Classify this cell by malaria status.
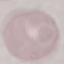

Uninfected.

Summary:
  - Image type: cell patch, automatically extracted from a larger field of view and resized to 64 × 64 pixels
  - Preparation: thin smear
  - Stain: Giemsa
  - Capture: smartphone through the microscope eyepiece